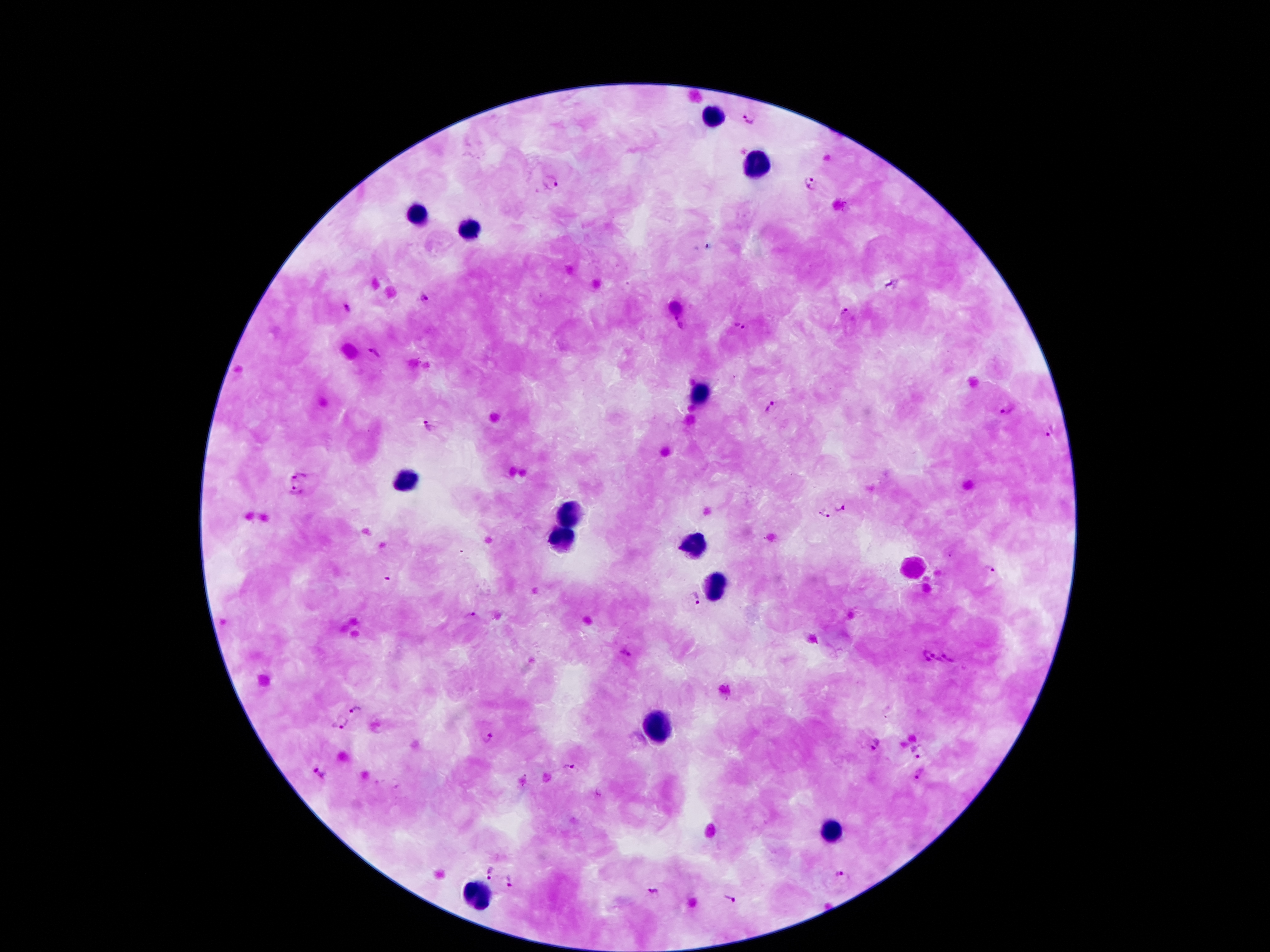 Single field of view. Photographed through the microscope eyepiece with a smartphone camera. Image is 1270×952 pixels. Thick peripheral-blood smear. Giemsa-stained preparation. 100x magnification. Patient malaria status: infected with Plasmodium falciparum.